State which cell type is depicted.
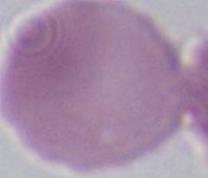

An erythrocyte.

magnification = 1000x
modality = micrograph